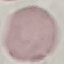
malaria status = uninfected
image type = cell patch, automatically extracted from a larger field of view and resized to 64 × 64 pixels
preparation = thin blood smear
stain = Giemsa
capture = smartphone through the microscope eyepiece